Outline each blood parasite and name the species.
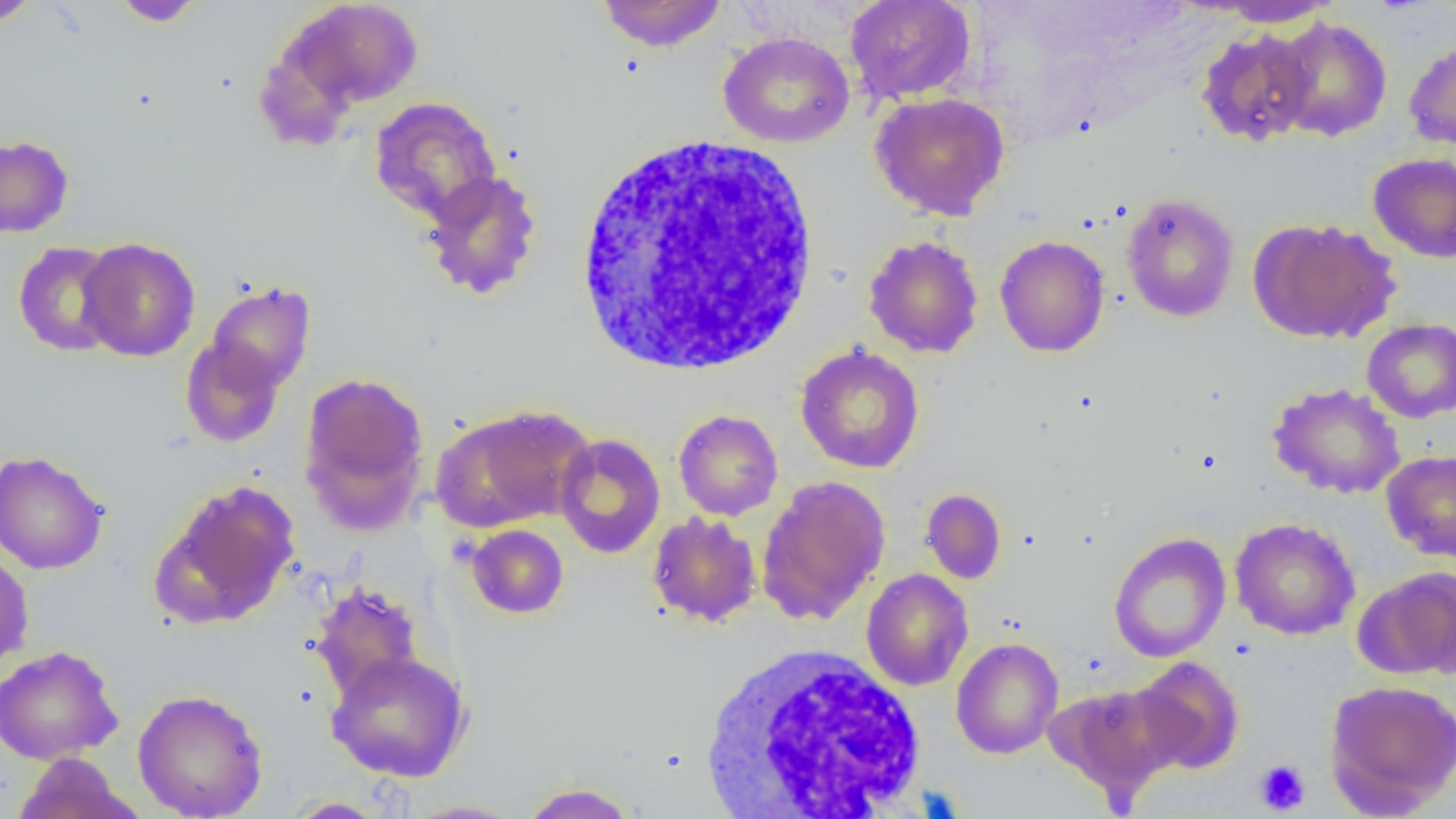

No blood parasites seen.

Approximate bounding boxes as named x1/y1/x2/y2 corners in pixels. Uninfected red blood cell locations: (x1=0, y1=0, x2=43, y2=27), (x1=595, y1=0, x2=728, y2=52), (x1=845, y1=0, x2=976, y2=104), (x1=111, y1=1, x2=207, y2=27), (x1=279, y1=1, x2=423, y2=113), (x1=1215, y1=1, x2=1341, y2=27), (x1=1273, y1=16, x2=1393, y2=142), (x1=1195, y1=28, x2=1317, y2=147), (x1=717, y1=31, x2=855, y2=148), (x1=1404, y1=38, x2=1456, y2=152), (x1=870, y1=92, x2=1010, y2=220), (x1=369, y1=96, x2=501, y2=224), (x1=0, y1=133, x2=74, y2=238), (x1=1368, y1=153, x2=1456, y2=263), (x1=419, y1=169, x2=543, y2=302), (x1=1122, y1=192, x2=1239, y2=322), (x1=1249, y1=217, x2=1399, y2=344), (x1=864, y1=235, x2=984, y2=358), (x1=995, y1=235, x2=1110, y2=358), (x1=77, y1=237, x2=200, y2=362), (x1=13, y1=241, x2=124, y2=357), (x1=203, y1=280, x2=316, y2=396), (x1=1362, y1=319, x2=1456, y2=423), (x1=180, y1=335, x2=287, y2=448), (x1=795, y1=344, x2=925, y2=473), (x1=299, y1=371, x2=430, y2=529), (x1=1267, y1=382, x2=1406, y2=498), (x1=432, y1=406, x2=592, y2=530), (x1=674, y1=409, x2=783, y2=520), (x1=554, y1=433, x2=665, y2=558), (x1=0, y1=450, x2=109, y2=575), (x1=1381, y1=450, x2=1456, y2=562), (x1=756, y1=475, x2=890, y2=625), (x1=152, y1=479, x2=301, y2=628), (x1=921, y1=488, x2=1006, y2=584), (x1=647, y1=512, x2=762, y2=627), (x1=1230, y1=517, x2=1360, y2=640), (x1=466, y1=524, x2=569, y2=619), (x1=1108, y1=532, x2=1231, y2=662), (x1=0, y1=548, x2=34, y2=675), (x1=1360, y1=566, x2=1456, y2=679), (x1=861, y1=569, x2=973, y2=691), (x1=309, y1=581, x2=424, y2=701), (x1=951, y1=637, x2=1064, y2=759), (x1=0, y1=645, x2=123, y2=764), (x1=326, y1=651, x2=471, y2=782), (x1=1132, y1=656, x2=1245, y2=775), (x1=1325, y1=678, x2=1456, y2=814), (x1=1048, y1=683, x2=1183, y2=804), (x1=132, y1=688, x2=269, y2=819), (x1=11, y1=752, x2=139, y2=819), (x1=517, y1=782, x2=640, y2=819), (x1=283, y1=797, x2=390, y2=818), (x1=401, y1=799, x2=526, y2=818). Platelet locations: (x1=1253, y1=759, x2=1311, y2=815). White blood cell locations: (x1=571, y1=132, x2=823, y2=377), (x1=698, y1=644, x2=931, y2=818). Slide-level diagnosis: negative for blood parasites. Thin blood film. One field of a larger specimen. Image is 1456×819 pixels. Light microscopy. Captured at 1000x magnification.